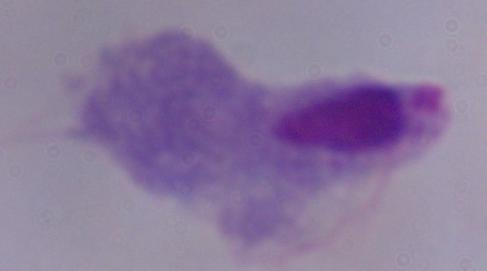

magnification: 1000x
modality: photomicrograph
identification: trichomonad